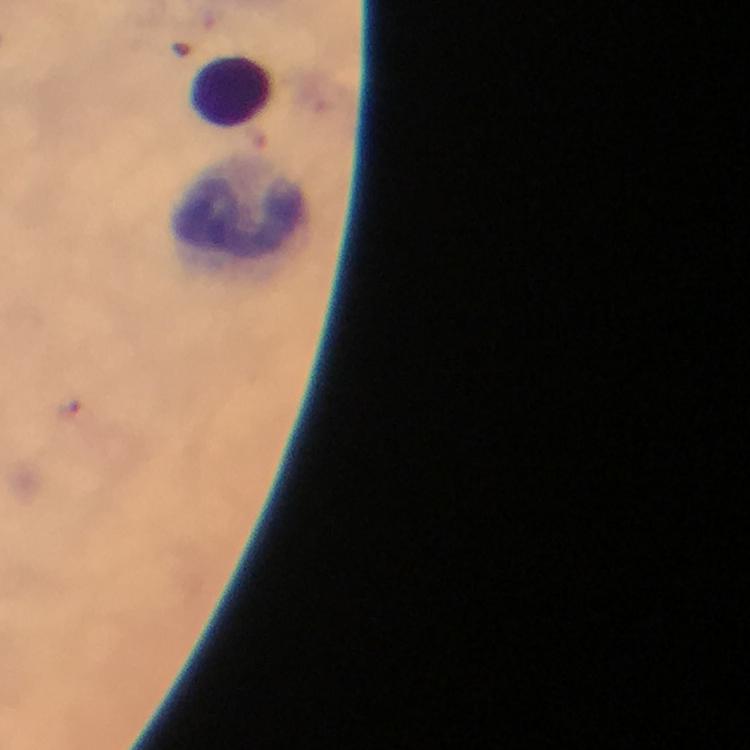
Approximate centers as [x, y] in pixels.
Summary:
  - Leukocyte locations: [234, 92], [242, 216]
  - Plasmodium parasite locations: [73, 412]
  - Immersion oil: applied
  - Context: from a diagnostic examination for malaria
  - Preparation: thick blood film
  - Stain: Giemsa
  - Image size: 750×750 pixels
  - Cropped from: a single field of view
  - Capture: smartphone photograph through a microscope
  - Magnification: 100x